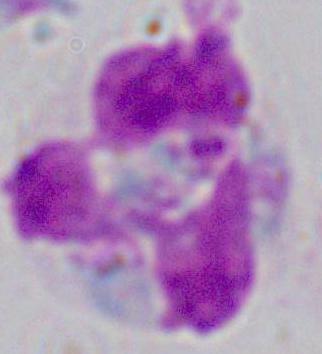
{
  "modality": "micrograph",
  "identification": "white blood cell",
  "magnification": "1000x"
}